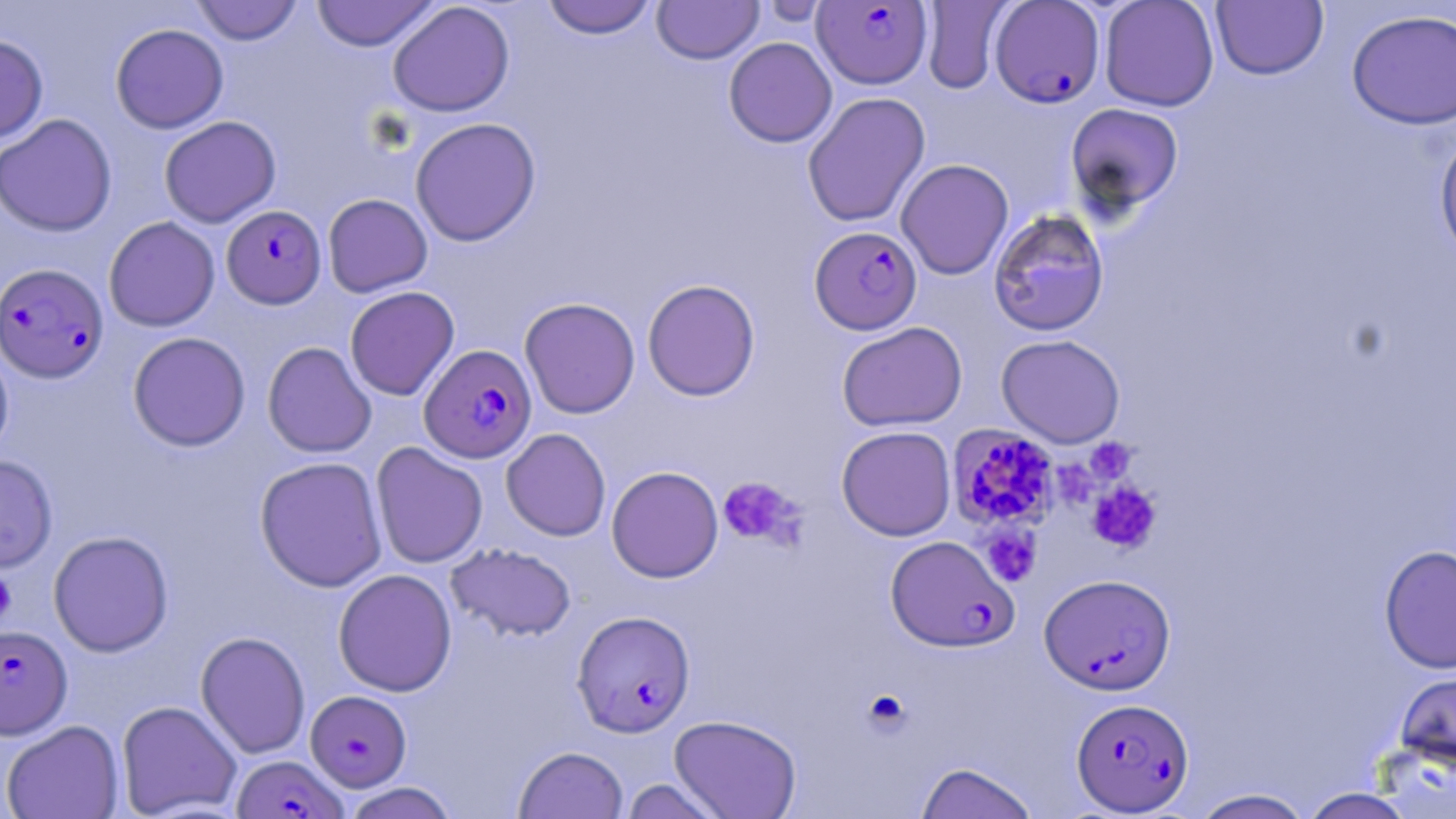
Plasmodium falciparum-infected red blood cell locations = approximate bounding boxes as (x1,y1)-(x2,y2) corner pairs in pixels: (812,1)-(932,89), (989,1)-(1105,108), (221,205)-(326,309), (810,226)-(922,335), (1,263)-(109,384), (419,344)-(537,463), (947,425)-(1061,531), (885,534)-(1019,652), (1039,573)-(1176,695), (571,610)-(695,737), (0,625)-(72,739), (305,690)-(411,791), (1071,698)-(1194,815), (232,754)-(346,818)
slide-level diagnosis = Plasmodium falciparum
uninfected red blood cell locations = approximate bounding boxes as (x1,y1)-(x2,y2) corner pairs in pixels: (190,0)-(304,45), (310,0)-(441,52), (540,0)-(658,39), (1099,0)-(1220,112), (651,1)-(764,64), (919,1)-(1014,93), (1211,1)-(1328,81), (387,2)-(515,117), (1346,8)-(1456,130), (110,24)-(229,133), (0,34)-(48,143), (723,37)-(837,147), (802,91)-(931,227), (1065,102)-(1184,217), (0,114)-(118,237), (159,115)-(281,227), (410,117)-(541,246), (1433,129)-(1456,265), (896,159)-(1014,280), (323,193)-(433,297), (987,208)-(1110,336), (103,216)-(220,332), (642,278)-(760,401), (345,286)-(459,401), (519,297)-(640,419), (837,321)-(968,432), (127,332)-(251,451), (996,334)-(1125,448), (262,341)-(376,458), (0,344)-(14,459), (836,425)-(956,541), (501,428)-(611,541), (370,442)-(488,569), (0,454)-(58,573), (254,456)-(389,593), (606,466)-(723,582), (48,530)-(174,657), (446,543)-(576,642), (1379,544)-(1456,673), (333,569)-(457,697), (195,631)-(310,758), (1393,667)-(1456,775), (116,700)-(242,818), (669,715)-(802,818), (1,720)-(124,819), (513,745)-(627,818), (916,762)-(1038,819), (619,777)-(727,819), (341,782)-(459,819), (1190,788)-(1315,818), (1299,788)-(1419,819)
image size = 1456×819 pixels
modality = optical microscopy
preparation = thin blood smear
field of view = single
platelet locations = approximate bounding boxes as (x1,y1)-(x2,y2) corner pairs in pixels: (718,476)-(802,547), (1087,482)-(1161,553), (980,526)-(1041,586), (0,570)-(17,626)
stain = May-Grünwald-Giemsa
magnification = 1000x